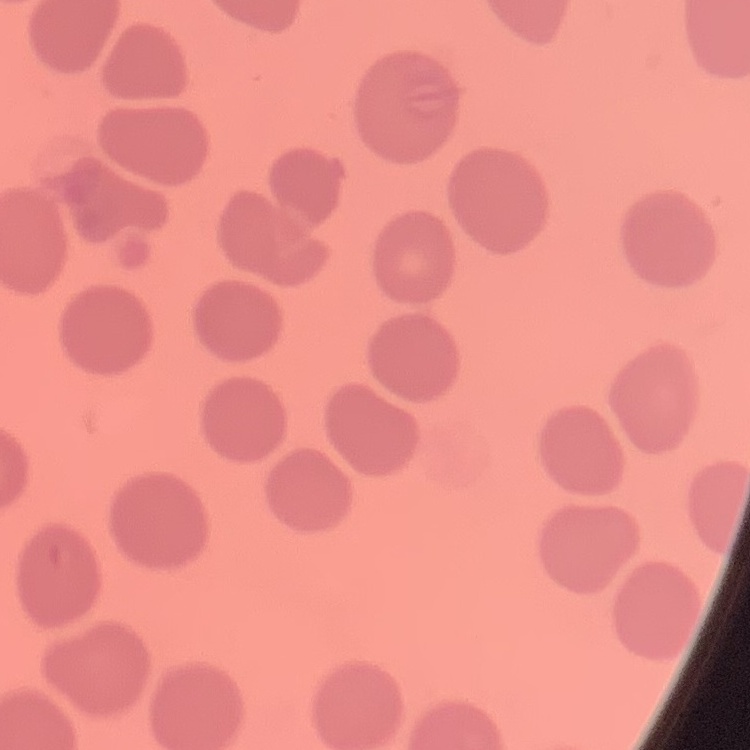

erythrocyte morphology = no rouleaux formation
preparation = thin blood smear
stain = Field's or Giemsa
image type = square crop of a larger photomicrograph